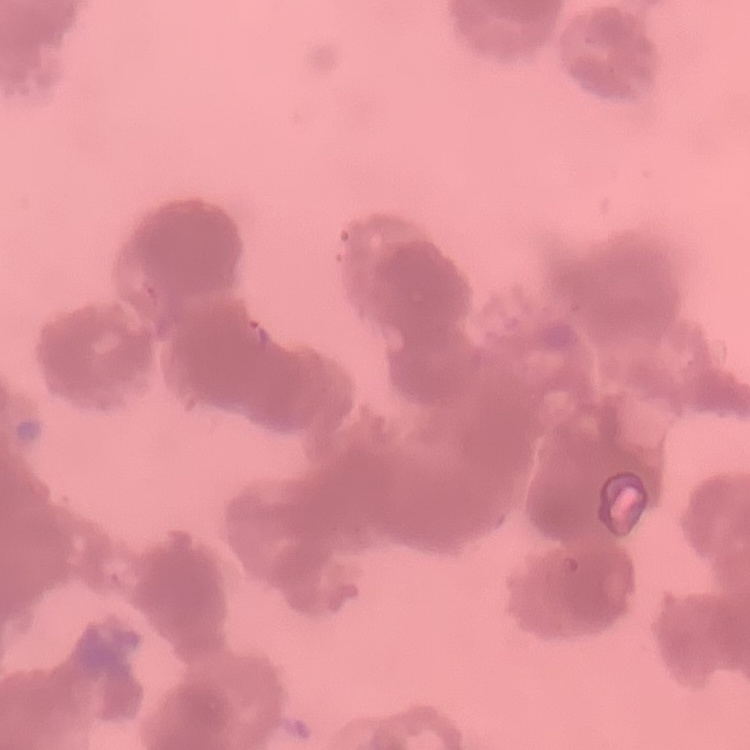

erythrocyte morphology = rouleaux formation
image type = one tile cut from a larger photomicrograph
preparation = thin blood film
stain = Field's or Giemsa